Locate every blood parasite and identify its species.
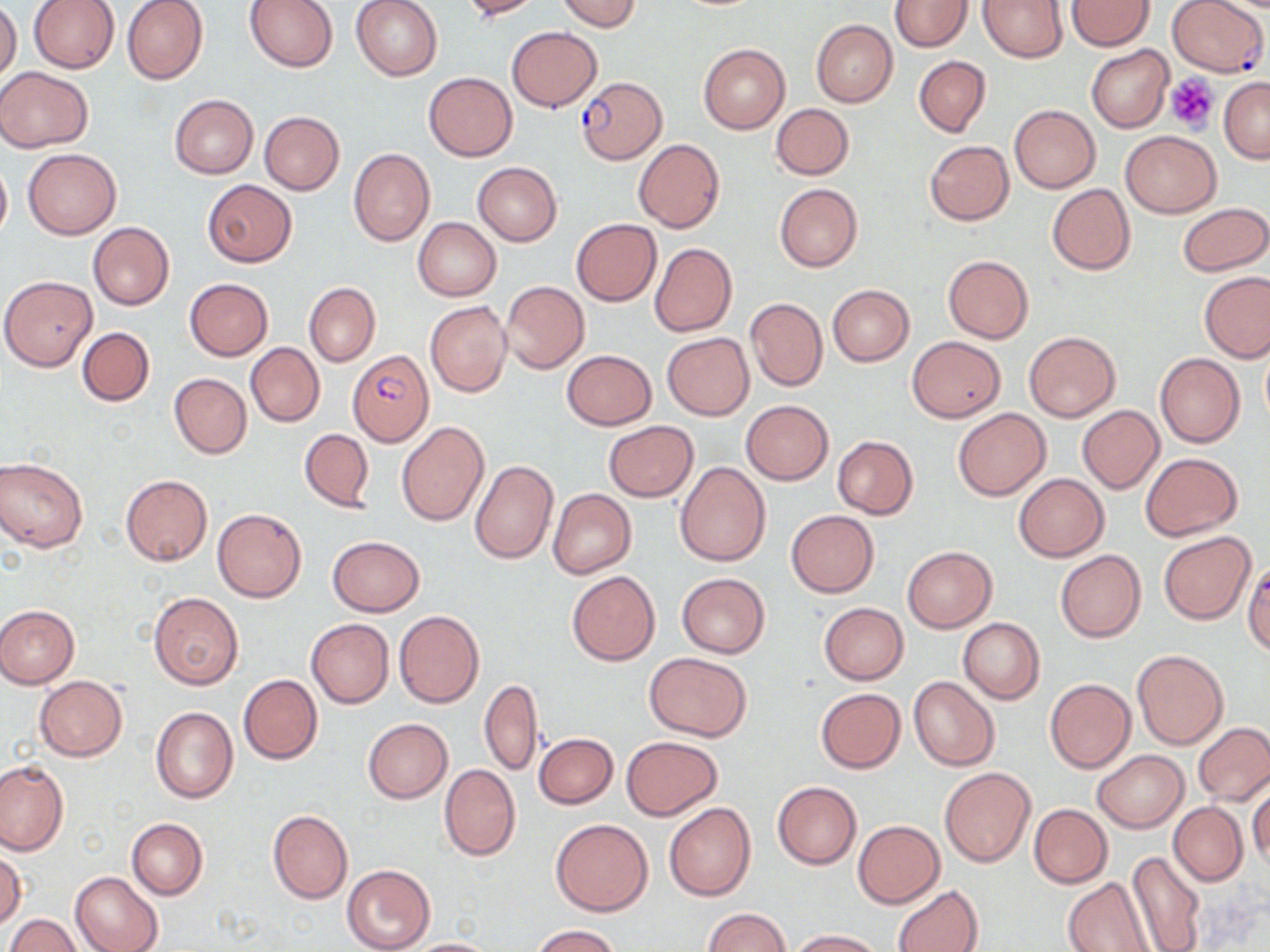
Approximate bounding boxes as (x1, y1, x2, y2) in pixels.
Plasmodium falciparum-infected red blood cells: (1169, 1, 1267, 78), (577, 78, 664, 164), (348, 351, 433, 445).
No Plasmodium ovale, Plasmodium malariae, Plasmodium vivax, Babesia divergens, or Trypanosoma brucei observed.

slide_level_diagnosis: Plasmodium falciparum
modality: optical microscopy
magnification: 1000x
field_of_view: one of a larger specimen
uninfected_red_blood_cell_locations: 'approximate bounding boxes as (x1, y1, x2, y2) in pixels: (122, 0, 208, 84), (245, 0, 338, 73), (351, 0, 444, 81), (458, 0, 542, 21), (557, 0, 641, 32), (979, 0, 1066, 62), (28, 1, 119, 73), (890, 1, 971, 51), (1066, 1, 1154, 51), (0, 3, 21, 85), (811, 19, 897, 106), (506, 26, 602, 111), (698, 44, 790, 134), (1087, 46, 1174, 133), (914, 55, 991, 136), (0, 66, 93, 153), (424, 72, 518, 160), (1219, 78, 1270, 164), (169, 94, 259, 178), (771, 103, 854, 180), (1010, 105, 1100, 192), (259, 112, 345, 195), (1121, 131, 1220, 217), (633, 139, 725, 232), (924, 140, 1014, 226), (348, 147, 435, 246), (23, 148, 121, 239), (0, 156, 11, 245), (472, 162, 562, 246), (202, 180, 297, 266), (774, 183, 863, 271), (1046, 184, 1135, 275), (1178, 202, 1270, 276), (413, 217, 500, 300), (571, 218, 661, 306), (88, 222, 174, 310), (650, 242, 738, 337), (943, 255, 1033, 343), (1200, 273, 1270, 362), (1, 275, 97, 370), (184, 278, 272, 361), (501, 280, 589, 374), (305, 282, 380, 366), (827, 285, 914, 366), (745, 298, 828, 391), (425, 301, 512, 398), (77, 326, 154, 406), (1024, 331, 1121, 422), (662, 333, 753, 420), (906, 337, 1005, 421), (245, 342, 324, 427), (1261, 344, 1270, 425), (562, 350, 656, 429), (1155, 353, 1246, 448), (170, 373, 251, 459), (740, 400, 833, 484), (1077, 405, 1164, 493), (953, 408, 1051, 501), (397, 421, 489, 526), (604, 421, 698, 501), (299, 429, 375, 512), (833, 435, 918, 518), (1140, 452, 1244, 541), (0, 458, 88, 552), (469, 459, 558, 564), (675, 461, 772, 566), (1013, 473, 1109, 561), (120, 475, 212, 566), (548, 489, 636, 578), (212, 508, 306, 603), (785, 510, 878, 597), (1158, 531, 1256, 625), (327, 535, 425, 616), (902, 546, 996, 631), (1055, 549, 1146, 643), (1242, 558, 1270, 656), (566, 571, 660, 665), (676, 572, 771, 658), (148, 591, 244, 690), (818, 602, 909, 684), (0, 605, 79, 688), (393, 611, 485, 709), (306, 618, 394, 708), (959, 618, 1045, 704), (1132, 650, 1229, 751), (645, 652, 752, 740), (239, 675, 323, 764), (34, 676, 128, 761), (909, 676, 1000, 771), (1045, 678, 1135, 772), (480, 679, 544, 776), (816, 687, 905, 773), (150, 707, 238, 803), (363, 718, 453, 802), (1192, 723, 1270, 805), (534, 732, 617, 808), (622, 736, 722, 819), (1092, 750, 1187, 832), (0, 761, 67, 855), (439, 765, 520, 860), (940, 768, 1035, 867), (1249, 779, 1269, 869), (771, 781, 860, 869), (664, 803, 755, 900), (1169, 803, 1248, 886), (1029, 804, 1112, 888), (267, 810, 353, 904), (127, 818, 207, 901), (550, 819, 653, 917), (853, 821, 945, 907), (0, 849, 26, 930), (1126, 849, 1206, 952), (342, 865, 434, 952), (71, 871, 163, 952), (1062, 877, 1155, 952), (893, 884, 984, 952), (702, 907, 791, 952), (6, 914, 82, 952), (529, 925, 621, 952), (786, 928, 883, 951), (404, 938, 500, 952)'
platelet_locations: 'approximate bounding boxes as (x1, y1, x2, y2) in pixels: (1166, 73, 1217, 136)'
preparation: thin blood smear
image_size: 1270×952 pixels
stain: May-Grünwald-Giemsa